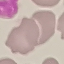 Malaria status: uninfected. Giemsa-stained preparation. Thin smear of blood. Automatically extracted cell patch, resized to 64 × 64 pixels. Photographed with a smartphone camera at the microscope eyepiece.